Assess this cell for malaria.
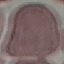

Uninfected.

Giemsa stain. Automatically extracted cell patch, resized to 64 × 64 pixels. Thin blood smear. Photographed with a smartphone camera at the microscope eyepiece.